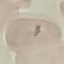

Result: no malaria parasites seen. Thin blood film. Giemsa-stained preparation. Cell patch, automatically extracted from a larger field of view and resized to 64 × 64 pixels. Photographed with a smartphone camera at the microscope eyepiece.